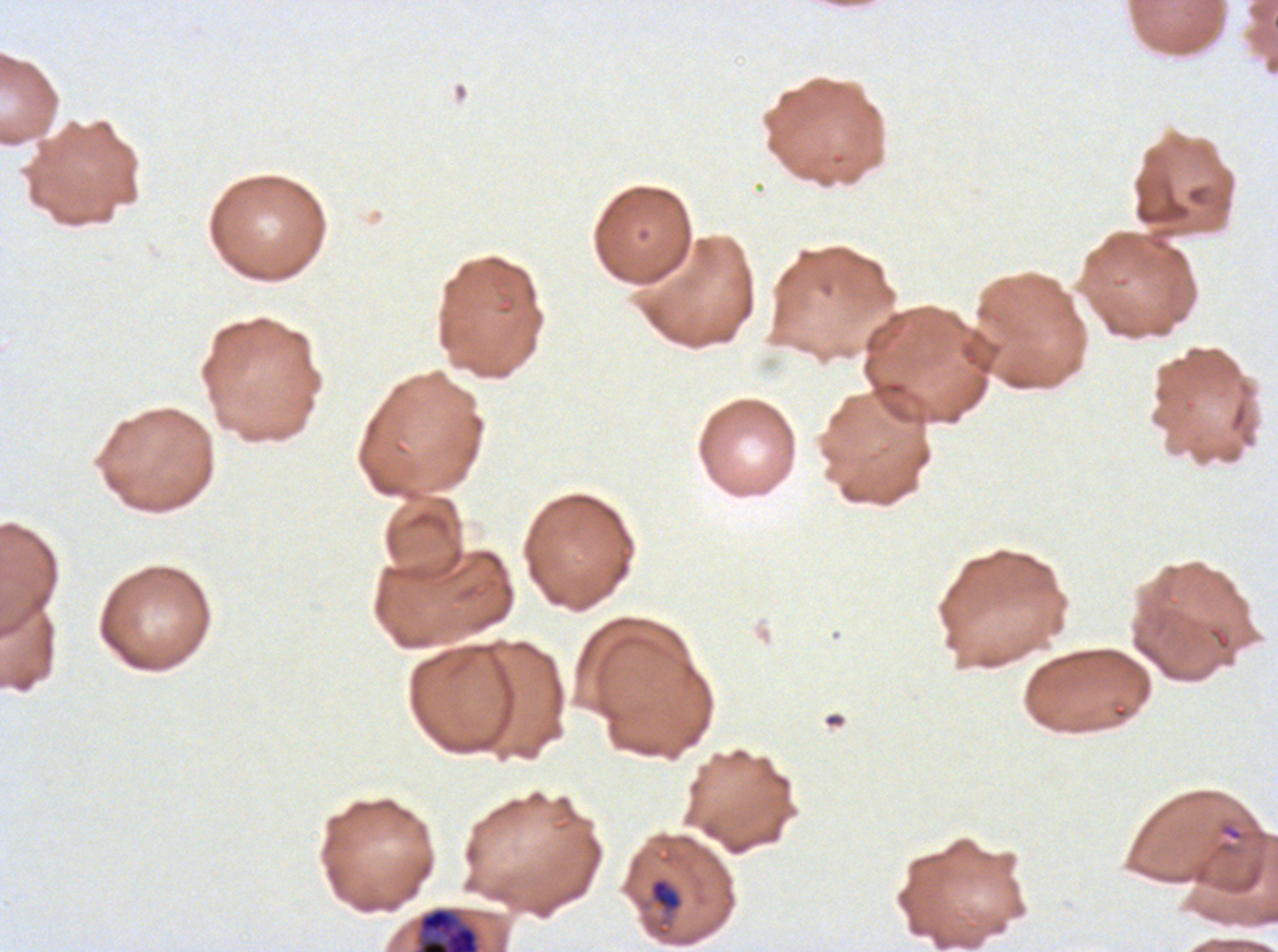
Approximate bounding boxes as {x1, y1, x2, y2} in pixels.
Summary:
  - Late-ring/early-trophozoite locations: {649, 878, 682, 911}
  - Early schizont locations: {416, 907, 481, 951}
  - Ring locations: {1222, 824, 1243, 841}
  - Stain: Giemsa
  - Preparation: thin blood film
  - Specimen: P. falciparum cultured ex vivo for 24 to 48 hours, from a patient in The Gambia
  - Field of view: one sub-image of a larger composite
  - Image size: 1278×952 pixels
  - Life-cycle stages observed: ring, late-ring/early-trophozoite, early schizont